Classify this cell by malaria status.
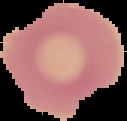
It is uninfected.

Summary:
  - Image size: 127×121 pixels
  - Preparation: thin blood film
  - Image type: segmented cell region with the area outside set to black